Comment on the morphology of the erythrocytes.
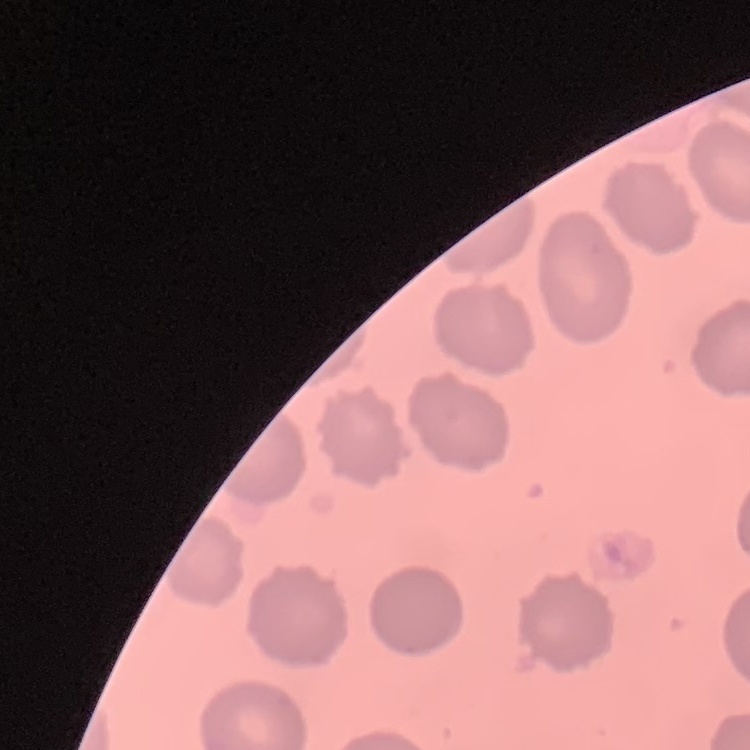
They show no rouleaux formation.

Summary:
  - Image type: one tile cut from a larger photomicrograph
  - Stain: Field's or Giemsa
  - Preparation: thin blood smear